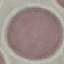
Summary:
  - Result: no malaria parasites seen
  - Capture: smartphone camera at the microscope eyepiece
  - Image type: cell patch, automatically extracted from a larger field of view and resized to 64 × 64 pixels
  - Preparation: thin blood smear
  - Stain: Giemsa